Locate every parasitized red blood cell.
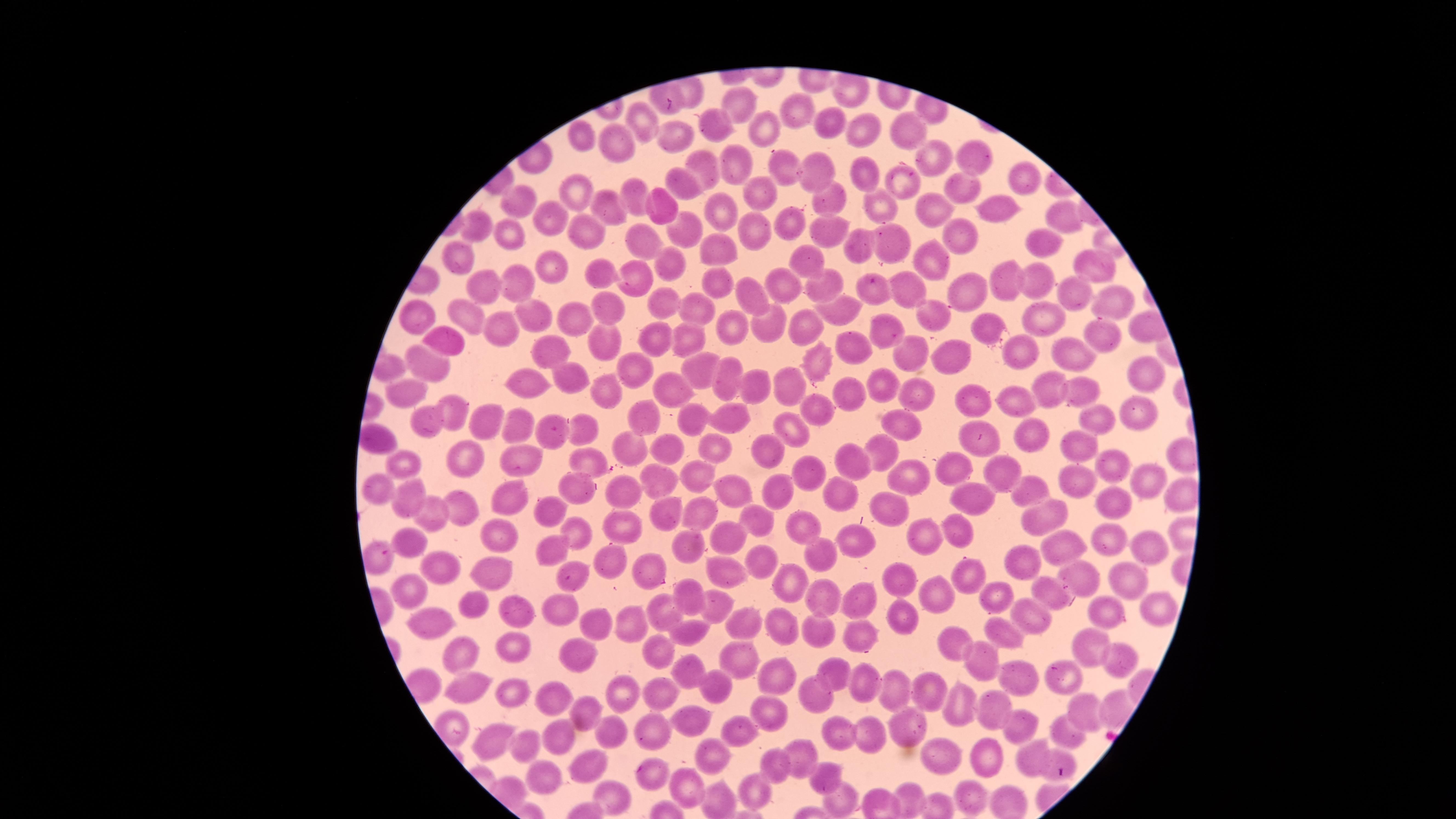

No parasitized red blood cells identified.

stain: Giemsa
field_of_view: single
capture: smartphone photograph through the microscope eyepiece
uninfected_red_blood_cells: 'approximate marker points, in pixels from the top-left corner: (x=740, y=105), (x=796, y=110), (x=644, y=120), (x=834, y=122), (x=713, y=123), (x=863, y=128), (x=579, y=129), (x=908, y=130), (x=764, y=131), (x=676, y=140), (x=612, y=141), (x=971, y=156), (x=739, y=157), (x=932, y=159), (x=784, y=167), (x=707, y=169), (x=819, y=169), (x=867, y=173), (x=901, y=175), (x=1017, y=176), (x=681, y=184), (x=960, y=188), (x=575, y=190), (x=634, y=191), (x=758, y=191), (x=875, y=195), (x=518, y=202), (x=830, y=203), (x=658, y=204), (x=984, y=206), (x=605, y=208), (x=933, y=209), (x=718, y=210), (x=1058, y=216), (x=551, y=218), (x=788, y=218), (x=474, y=223), (x=581, y=227), (x=825, y=228), (x=678, y=230), (x=755, y=230), (x=512, y=231), (x=960, y=233), (x=901, y=238), (x=1044, y=242), (x=647, y=243), (x=719, y=243), (x=860, y=250), (x=452, y=256), (x=804, y=259), (x=674, y=261), (x=933, y=262), (x=551, y=265), (x=604, y=267), (x=1093, y=268), (x=519, y=280), (x=1037, y=280), (x=778, y=281), (x=634, y=282), (x=491, y=283), (x=905, y=284), (x=1010, y=284), (x=718, y=285), (x=824, y=286), (x=969, y=289), (x=872, y=290), (x=748, y=292), (x=1114, y=295), (x=1074, y=296), (x=610, y=303), (x=661, y=304), (x=695, y=309), (x=842, y=311), (x=422, y=313), (x=1037, y=313), (x=468, y=315), (x=536, y=316), (x=931, y=316), (x=573, y=317), (x=728, y=327), (x=767, y=327), (x=801, y=327), (x=884, y=327), (x=494, y=329), (x=993, y=330), (x=1098, y=334), (x=686, y=335), (x=445, y=336), (x=599, y=340), (x=658, y=342), (x=549, y=345), (x=851, y=348), (x=912, y=350), (x=1070, y=353), (x=1021, y=355), (x=958, y=359), (x=424, y=360), (x=691, y=364), (x=817, y=364), (x=1146, y=369), (x=634, y=372), (x=567, y=373), (x=724, y=378), (x=528, y=381), (x=783, y=382), (x=1044, y=385), (x=673, y=386), (x=879, y=386), (x=757, y=387), (x=915, y=390), (x=409, y=393), (x=608, y=393), (x=848, y=393), (x=1083, y=393), (x=970, y=398), (x=1011, y=403), (x=456, y=408), (x=733, y=410), (x=1138, y=410), (x=822, y=412), (x=646, y=415), (x=1093, y=418), (x=489, y=420), (x=901, y=420), (x=693, y=421), (x=424, y=422), (x=589, y=423), (x=792, y=426), (x=517, y=428), (x=1033, y=429), (x=555, y=430), (x=984, y=438), (x=712, y=445), (x=1074, y=446), (x=762, y=447), (x=628, y=449), (x=666, y=450), (x=883, y=451), (x=459, y=456), (x=855, y=457), (x=523, y=460), (x=583, y=461), (x=405, y=464), (x=958, y=466), (x=1112, y=468), (x=697, y=471), (x=807, y=475), (x=908, y=475), (x=1001, y=476), (x=1147, y=476), (x=658, y=484), (x=1080, y=484), (x=731, y=485), (x=1028, y=485), (x=778, y=488), (x=576, y=489), (x=624, y=493), (x=836, y=493), (x=373, y=498), (x=508, y=498), (x=974, y=499), (x=413, y=502), (x=888, y=503), (x=1111, y=504), (x=556, y=508), (x=459, y=509), (x=701, y=509), (x=1040, y=513), (x=429, y=518), (x=667, y=518), (x=755, y=518), (x=623, y=524), (x=803, y=528), (x=958, y=528), (x=574, y=535), (x=922, y=535), (x=504, y=537), (x=853, y=538), (x=729, y=539), (x=406, y=540), (x=688, y=540), (x=1113, y=540), (x=1068, y=543), (x=561, y=549), (x=1148, y=549), (x=825, y=555), (x=376, y=560), (x=1025, y=561), (x=759, y=562), (x=612, y=565), (x=643, y=565), (x=438, y=567), (x=719, y=568), (x=491, y=571), (x=1079, y=574), (x=963, y=575), (x=570, y=577), (x=903, y=579), (x=1132, y=581), (x=788, y=583), (x=1045, y=586), (x=408, y=588), (x=945, y=594), (x=689, y=596), (x=996, y=596), (x=826, y=597), (x=865, y=602), (x=474, y=603), (x=516, y=605), (x=713, y=605), (x=1154, y=605), (x=558, y=610), (x=1105, y=612), (x=906, y=613), (x=667, y=614), (x=1033, y=616), (x=434, y=618), (x=631, y=620), (x=595, y=622), (x=747, y=626), (x=789, y=626), (x=1005, y=631), (x=825, y=632), (x=865, y=635), (x=690, y=636), (x=955, y=640), (x=658, y=644), (x=510, y=645), (x=1093, y=648), (x=467, y=649), (x=984, y=654), (x=582, y=656), (x=1119, y=659), (x=739, y=661), (x=831, y=666), (x=1019, y=674), (x=784, y=675), (x=683, y=676), (x=1061, y=678), (x=862, y=679), (x=714, y=683), (x=474, y=685), (x=630, y=688), (x=657, y=689), (x=512, y=691), (x=896, y=691), (x=929, y=692), (x=808, y=693), (x=556, y=696), (x=960, y=700), (x=1081, y=709), (x=999, y=710), (x=767, y=712), (x=586, y=714), (x=690, y=719), (x=652, y=724), (x=610, y=725), (x=1023, y=725), (x=907, y=727), (x=738, y=728), (x=838, y=731), (x=871, y=734), (x=1062, y=734), (x=493, y=736), (x=556, y=736), (x=525, y=746), (x=798, y=752), (x=711, y=754), (x=948, y=754), (x=995, y=756), (x=1036, y=760), (x=597, y=763), (x=776, y=763), (x=1051, y=769), (x=652, y=771), (x=825, y=775), (x=548, y=776), (x=686, y=787), (x=750, y=789), (x=970, y=793), (x=611, y=799), (x=913, y=799), (x=843, y=800)'
visible_region: circular
image_size: 1456×819 pixels
preparation: thin blood film